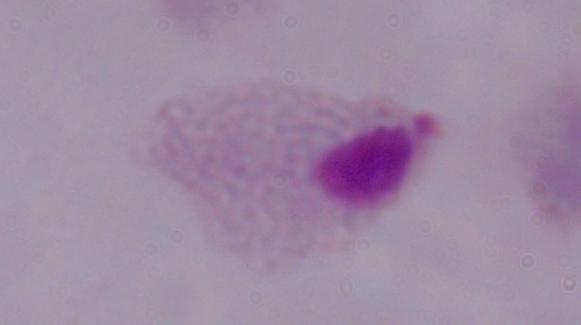

Summary:
  - Magnification: 1000x
  - Identification: trichomonad
  - Modality: micrograph